Classify this cell by malaria status.
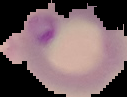
It is parasitized.

Summary:
  - Image size: 127×97 pixels
  - Image type: segmented cell region with the area outside set to black
  - Preparation: thin blood film